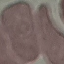
Summary:
  - Result: negative for malaria parasites
  - Capture: smartphone camera at the microscope eyepiece
  - Image type: cell patch, automatically extracted from a larger field of view and resized to 64 × 64 pixels
  - Stain: Giemsa
  - Preparation: thin smear